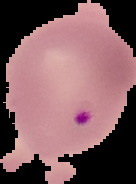

image_type: cell region segmented out of the field of view; surrounding area masked to black
image_size: 136×184 pixels
preparation: thin blood smear
malaria_status: parasitized